Report the malaria status of this cell.
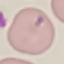

Uninfected.

Thin blood film. Cell patch, automatically extracted from a larger field of view and resized to 64 × 64 pixels. Giemsa stain. Photographed with a smartphone camera at the microscope eyepiece.